State the blood parasite species.
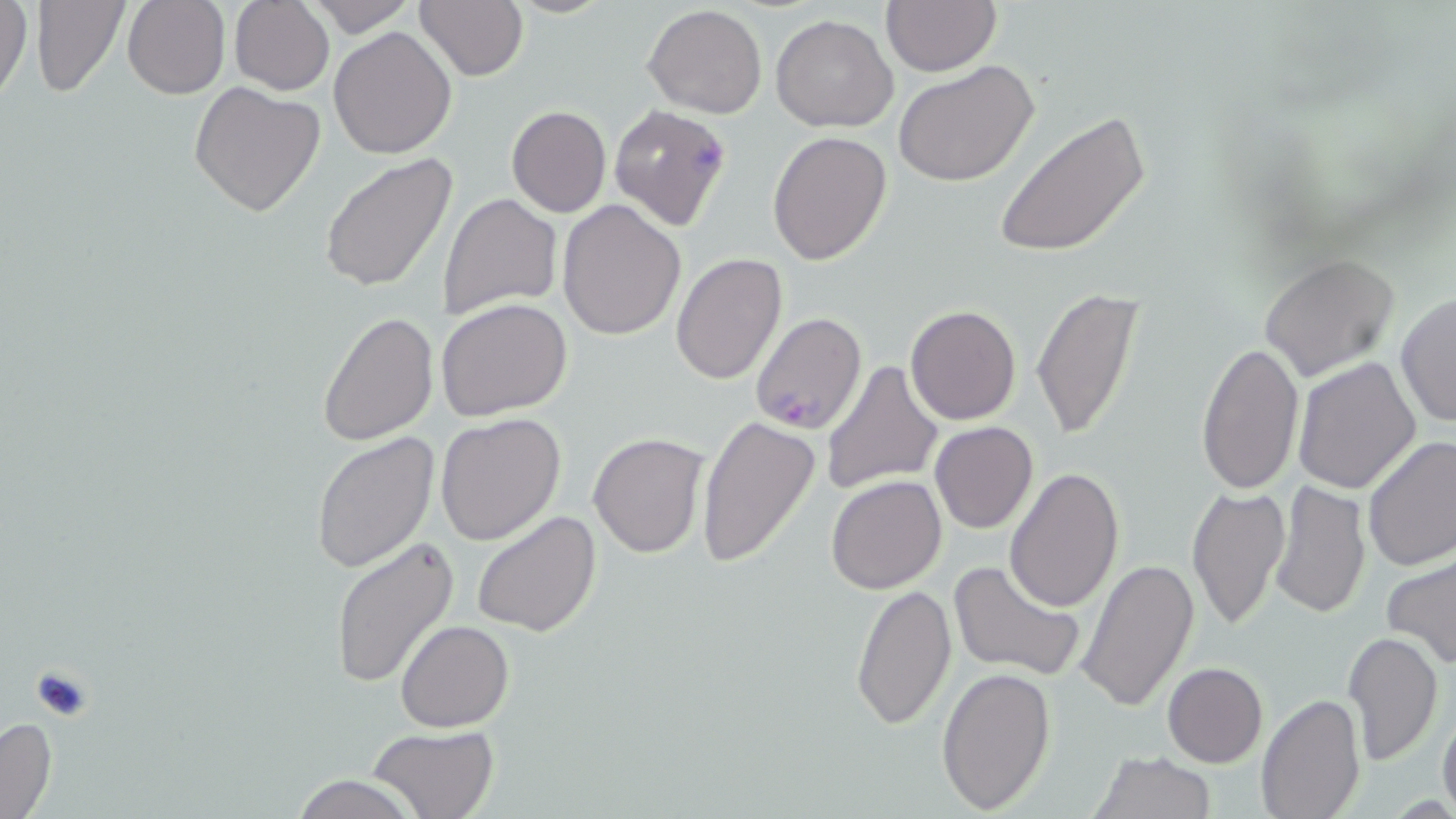
Plasmodium falciparum.

{
  "image_size": "1456×819 pixels",
  "uninfected_red_blood_cell_locations": "approximate bounding boxes as [x1, y1, x2, y2] in pixels: [2, 0, 32, 108], [29, 0, 131, 97], [123, 0, 229, 99], [307, 0, 416, 37], [414, 0, 528, 82], [505, 0, 615, 18], [881, 0, 1001, 76], [229, 1, 335, 95], [644, 4, 767, 117], [771, 15, 897, 133], [328, 26, 459, 158], [895, 59, 1040, 188], [189, 81, 327, 217], [506, 105, 611, 218], [993, 111, 1152, 259], [462, 124, 582, 276], [766, 131, 892, 265], [319, 155, 458, 292], [438, 193, 562, 321], [557, 199, 686, 340], [670, 253, 788, 385], [1259, 253, 1399, 383], [1030, 287, 1143, 441], [1394, 292, 1455, 429], [437, 299, 573, 422], [905, 305, 1023, 426], [317, 311, 438, 446], [1196, 340, 1302, 492], [1293, 356, 1422, 494], [821, 358, 944, 496], [435, 411, 566, 546], [696, 415, 819, 570], [929, 421, 1039, 534], [589, 431, 708, 558], [312, 433, 439, 577], [1362, 436, 1456, 572], [1004, 467, 1125, 615], [825, 475, 947, 593], [1269, 482, 1370, 618], [1186, 484, 1288, 631], [472, 511, 602, 639], [330, 537, 461, 689], [1382, 554, 1455, 671], [947, 557, 1084, 681], [1075, 558, 1200, 711], [850, 582, 957, 731], [395, 620, 513, 732], [1342, 629, 1443, 767], [1162, 662, 1268, 767], [936, 667, 1056, 815], [1257, 693, 1366, 819], [1436, 705, 1456, 819], [0, 717, 57, 819], [366, 725, 498, 819], [1088, 750, 1216, 819], [287, 774, 421, 818]",
  "stain": "May-Grünwald-Giemsa",
  "field_of_view": "one of a larger specimen",
  "modality": "optical microscopy",
  "plasmodium_falciparum_infected_red_blood_cell_locations": "approximate bounding boxes as [x1, y1, x2, y2] in pixels: [609, 103, 732, 231], [749, 312, 868, 433]",
  "magnification": "1000x",
  "preparation": "thin blood film"
}